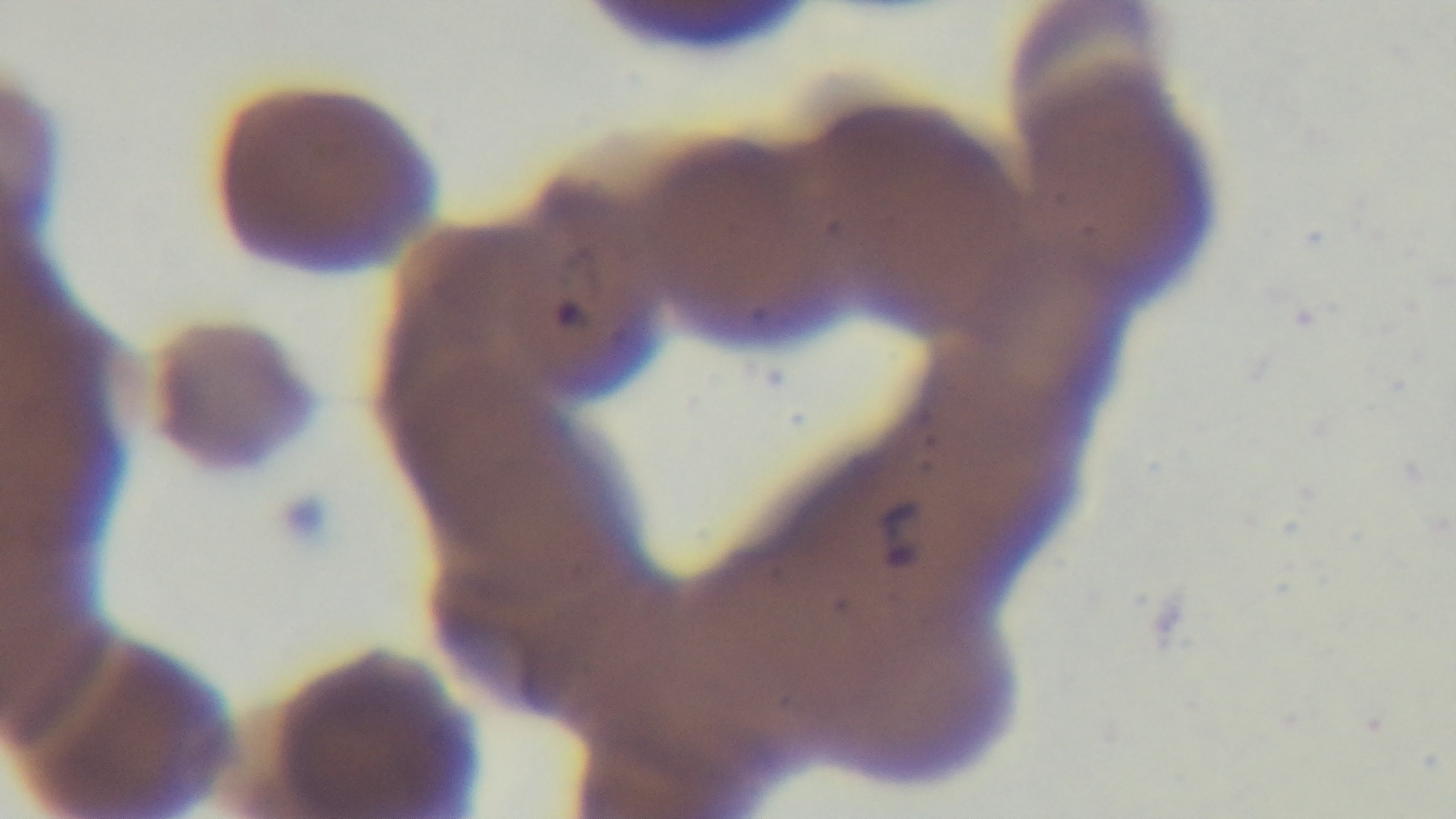
modality = light microscopy
objective = 100x oil immersion
stain = Giemsa
preparation = thin
malaria status = positive
capture = mounted 4K digital camera
field of view = single